Report the malaria status.
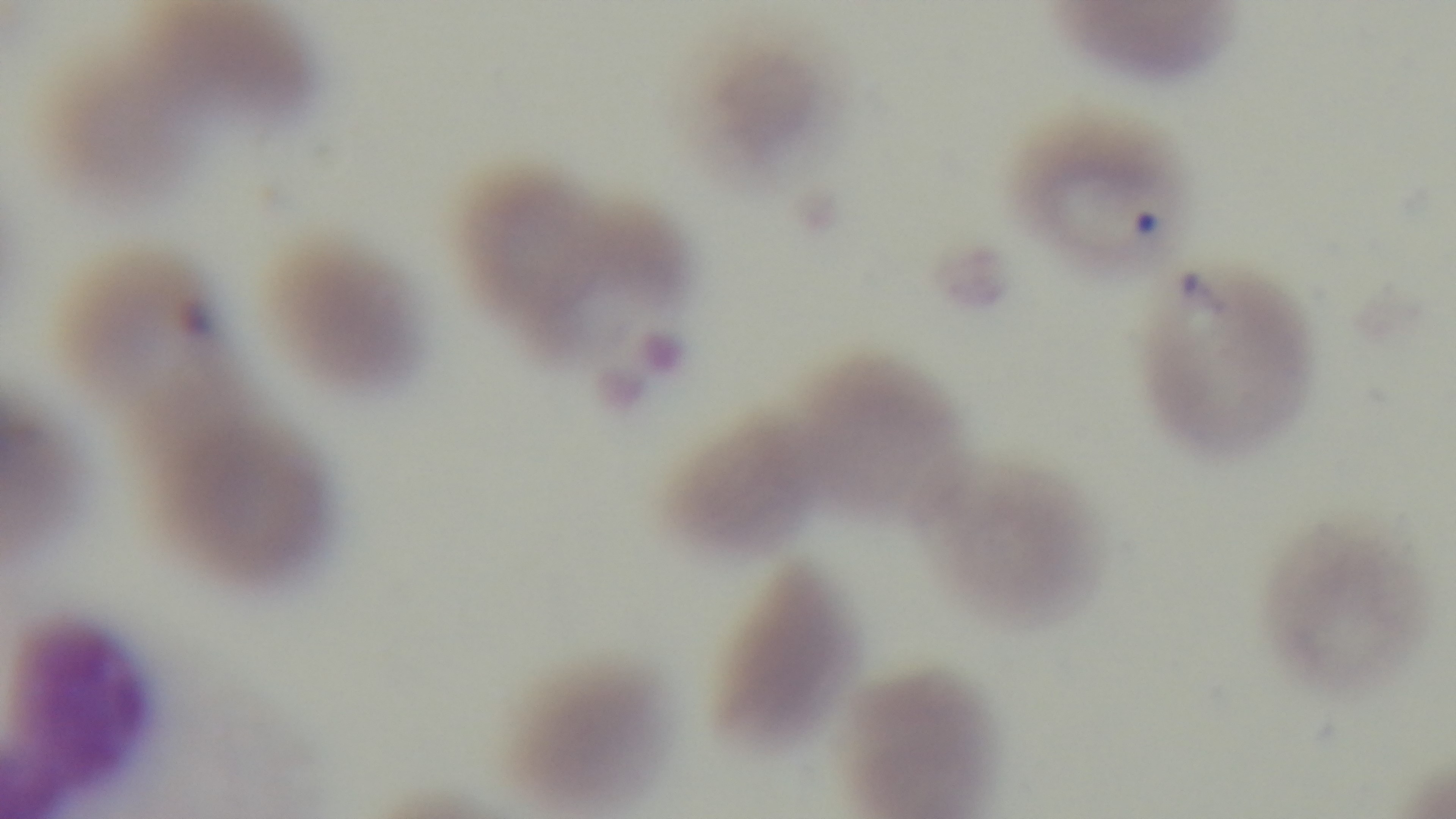

Positive.

objective: 100x oil immersion
preparation: thin blood film
capture: mounted 4K digital camera
stain: Giemsa
modality: light microscopy
field_of_view: single